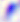
magnification = 400x
identification = Toxoplasma gondii
modality = photomicrograph